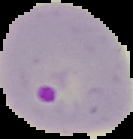
Summary:
  - Image size: 133×139 pixels
  - Image type: segmented cell region with the area outside set to black
  - Malaria status: parasitized
  - Preparation: thin blood smear